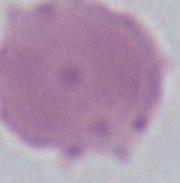

Summary:
  - Identification: red blood cell
  - Magnification: 1000x
  - Modality: photomicrograph